Look for Plasmodium parasites.
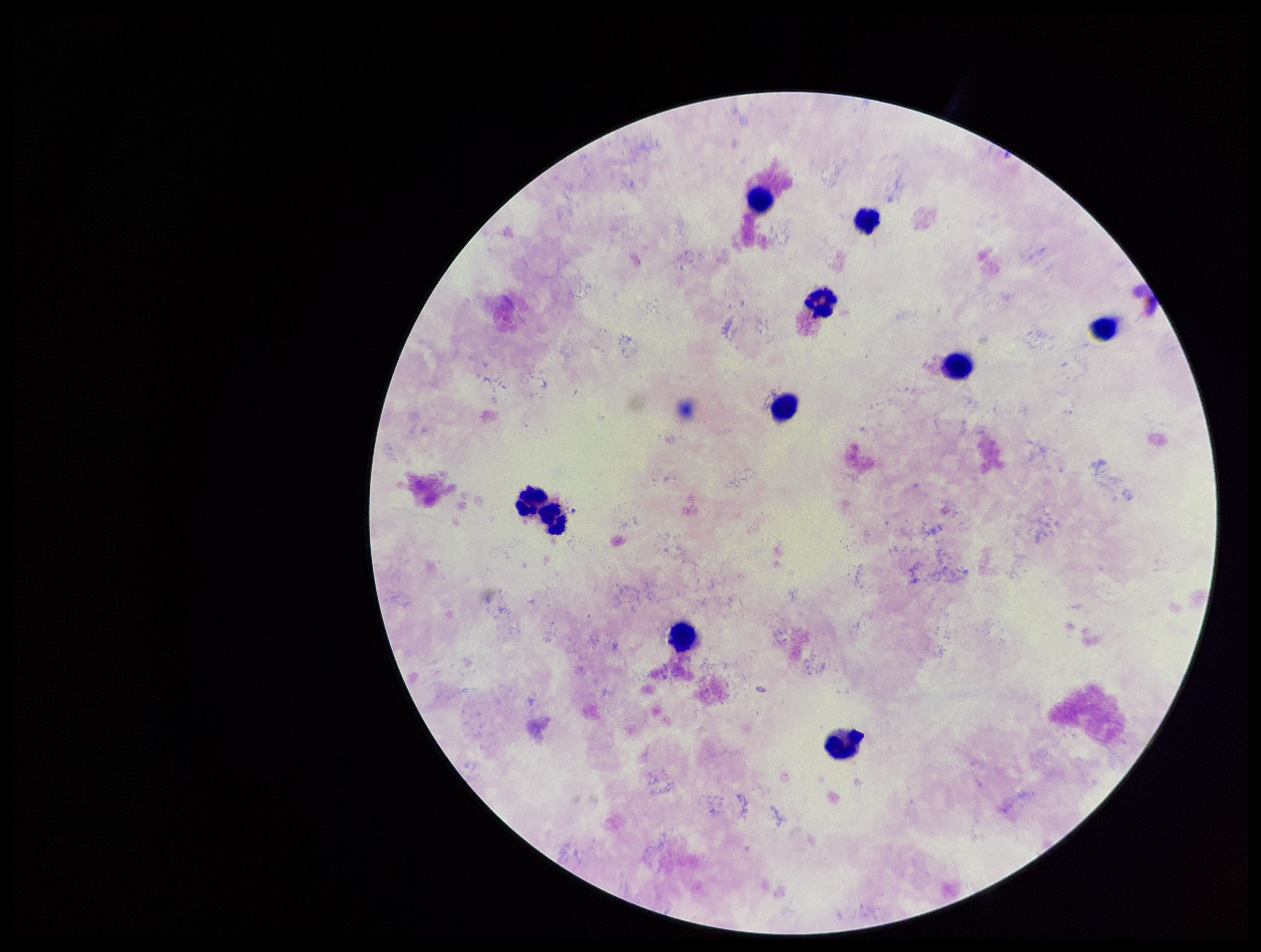
None identified.

Parasite count: 0. Smartphone photograph taken through the eyepiece of a microscope. Leukocyte count: 10. Image is 1261×952 pixels. Patient malaria status: positive. Species reported for this patient: Plasmodium falciparum. Single field of view. Giemsa stain. Preparation: thick blood smear.